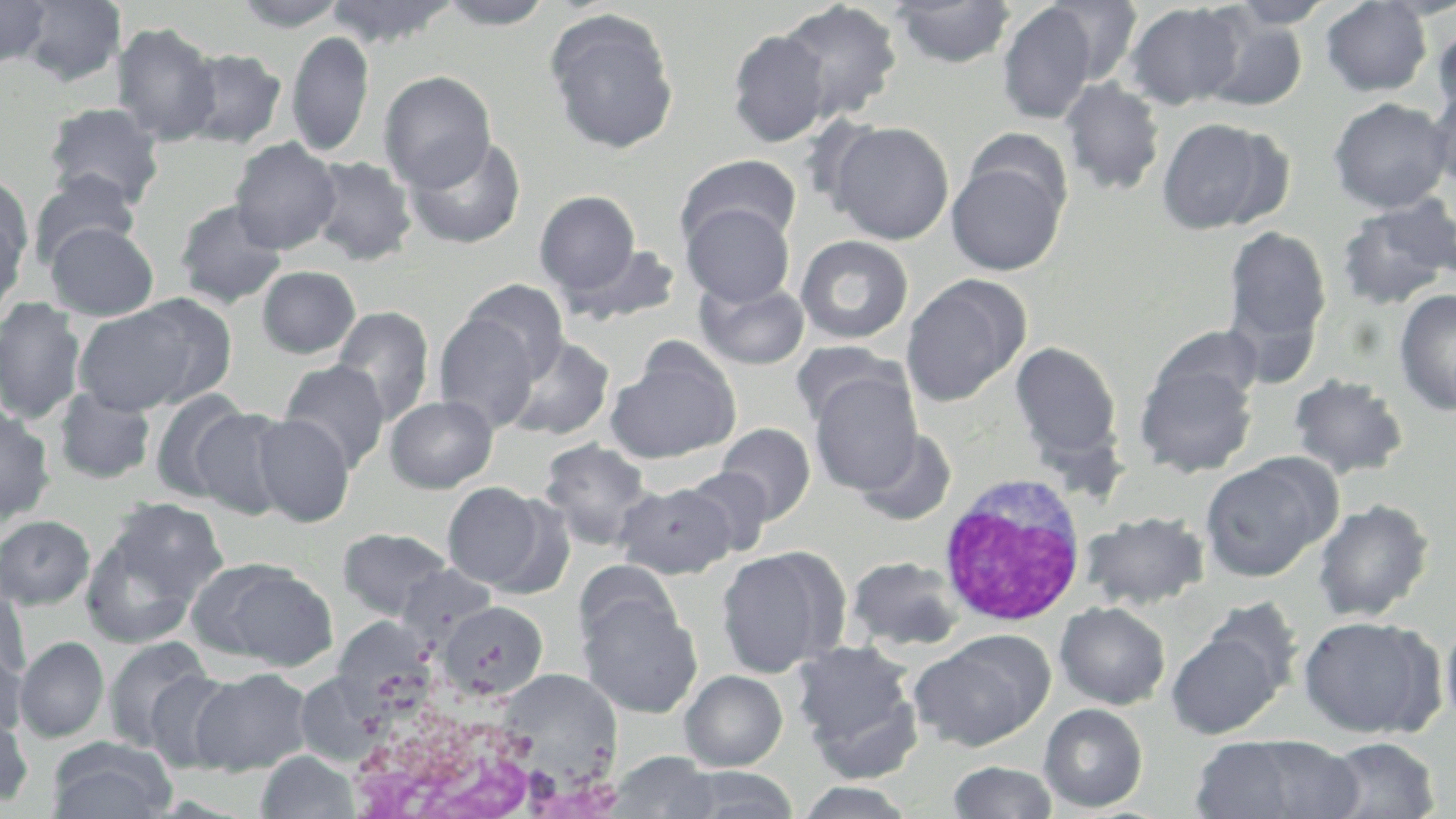
{
  "slide_level_diagnosis": "no evidence of blood parasites",
  "uninfected_red_blood_cell_locations": "approximate bounding boxes as named x1/y1/x2/y2 corners in pixels: (x1=0, y1=0, x2=51, y2=69), (x1=18, y1=0, x2=127, y2=87), (x1=231, y1=0, x2=350, y2=31), (x1=325, y1=0, x2=458, y2=47), (x1=434, y1=0, x2=556, y2=29), (x1=890, y1=0, x2=1015, y2=68), (x1=1042, y1=0, x2=1142, y2=86), (x1=1319, y1=0, x2=1433, y2=96), (x1=1226, y1=1, x2=1335, y2=29), (x1=776, y1=2, x2=903, y2=122), (x1=997, y1=3, x2=1100, y2=124), (x1=1123, y1=3, x2=1246, y2=109), (x1=545, y1=9, x2=680, y2=154), (x1=1199, y1=12, x2=1309, y2=112), (x1=1431, y1=18, x2=1456, y2=121), (x1=112, y1=22, x2=222, y2=145), (x1=726, y1=28, x2=831, y2=147), (x1=287, y1=31, x2=375, y2=158), (x1=181, y1=48, x2=287, y2=148), (x1=378, y1=71, x2=496, y2=191), (x1=1060, y1=78, x2=1166, y2=196), (x1=1427, y1=84, x2=1456, y2=192), (x1=1328, y1=97, x2=1453, y2=213), (x1=42, y1=102, x2=166, y2=208), (x1=1155, y1=117, x2=1283, y2=234), (x1=826, y1=120, x2=955, y2=244), (x1=405, y1=135, x2=526, y2=249), (x1=229, y1=138, x2=342, y2=254), (x1=676, y1=154, x2=801, y2=253), (x1=308, y1=156, x2=418, y2=266), (x1=946, y1=159, x2=1067, y2=276), (x1=28, y1=169, x2=141, y2=268), (x1=0, y1=172, x2=34, y2=272), (x1=535, y1=190, x2=641, y2=298), (x1=1335, y1=196, x2=1455, y2=310), (x1=174, y1=198, x2=288, y2=310), (x1=681, y1=202, x2=795, y2=307), (x1=0, y1=210, x2=26, y2=321), (x1=45, y1=222, x2=160, y2=320), (x1=1221, y1=224, x2=1332, y2=364), (x1=795, y1=235, x2=914, y2=344), (x1=562, y1=243, x2=681, y2=327), (x1=257, y1=265, x2=361, y2=359), (x1=900, y1=274, x2=1030, y2=407), (x1=460, y1=279, x2=569, y2=381), (x1=695, y1=279, x2=809, y2=369), (x1=1393, y1=289, x2=1456, y2=417), (x1=0, y1=297, x2=86, y2=425), (x1=72, y1=301, x2=214, y2=415), (x1=331, y1=306, x2=434, y2=425), (x1=433, y1=312, x2=539, y2=433), (x1=1147, y1=326, x2=1266, y2=413), (x1=501, y1=335, x2=615, y2=441), (x1=790, y1=340, x2=903, y2=430), (x1=1009, y1=341, x2=1124, y2=469), (x1=605, y1=344, x2=741, y2=464), (x1=279, y1=360, x2=391, y2=472), (x1=1134, y1=361, x2=1258, y2=478), (x1=809, y1=370, x2=923, y2=495), (x1=1289, y1=374, x2=1409, y2=479), (x1=53, y1=387, x2=155, y2=483), (x1=149, y1=389, x2=253, y2=502), (x1=385, y1=394, x2=498, y2=493), (x1=0, y1=405, x2=56, y2=524), (x1=190, y1=407, x2=294, y2=518), (x1=251, y1=414, x2=355, y2=527), (x1=716, y1=423, x2=815, y2=525), (x1=856, y1=429, x2=958, y2=526), (x1=537, y1=438, x2=655, y2=552), (x1=1200, y1=454, x2=1339, y2=583), (x1=682, y1=467, x2=775, y2=557), (x1=442, y1=481, x2=551, y2=589), (x1=614, y1=482, x2=736, y2=578), (x1=1312, y1=499, x2=1434, y2=622), (x1=79, y1=504, x2=225, y2=646), (x1=1081, y1=510, x2=1210, y2=610), (x1=0, y1=514, x2=96, y2=610), (x1=337, y1=528, x2=453, y2=620), (x1=717, y1=547, x2=844, y2=677), (x1=845, y1=556, x2=967, y2=652), (x1=189, y1=558, x2=338, y2=671), (x1=395, y1=564, x2=498, y2=636), (x1=0, y1=585, x2=32, y2=684), (x1=579, y1=595, x2=703, y2=717), (x1=439, y1=600, x2=548, y2=699), (x1=1054, y1=601, x2=1171, y2=709), (x1=1296, y1=614, x2=1444, y2=739), (x1=1441, y1=614, x2=1456, y2=733), (x1=336, y1=623, x2=432, y2=719), (x1=1166, y1=626, x2=1287, y2=739), (x1=908, y1=630, x2=1054, y2=752), (x1=102, y1=635, x2=213, y2=753), (x1=15, y1=637, x2=109, y2=743), (x1=790, y1=638, x2=924, y2=770), (x1=0, y1=646, x2=27, y2=739), (x1=191, y1=667, x2=313, y2=775), (x1=145, y1=669, x2=240, y2=772), (x1=492, y1=670, x2=625, y2=778), (x1=679, y1=670, x2=788, y2=771), (x1=302, y1=671, x2=389, y2=751), (x1=1039, y1=703, x2=1147, y2=813), (x1=0, y1=709, x2=34, y2=808), (x1=1191, y1=734, x2=1363, y2=819), (x1=1320, y1=736, x2=1441, y2=818), (x1=47, y1=738, x2=177, y2=819), (x1=256, y1=750, x2=361, y2=819), (x1=606, y1=752, x2=725, y2=819), (x1=946, y1=760, x2=1059, y2=819), (x1=676, y1=767, x2=800, y2=818), (x1=794, y1=782, x2=917, y2=818)",
  "preparation": "thin blood film",
  "field_of_view": "single",
  "white_blood_cell_locations": "approximate bounding boxes as named x1/y1/x2/y2 corners in pixels: (x1=934, y1=474, x2=1089, y2=627), (x1=351, y1=718, x2=605, y2=819)",
  "modality": "optical microscopy",
  "image_size": "1456×819 pixels",
  "magnification": "1000x",
  "stain": "May-Grünwald-Giemsa"
}